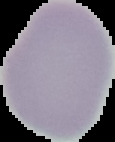

The area outside the segmented cell region is set to black. Image is 115×142 pixels. Malaria status: uninfected. From a thin blood film.